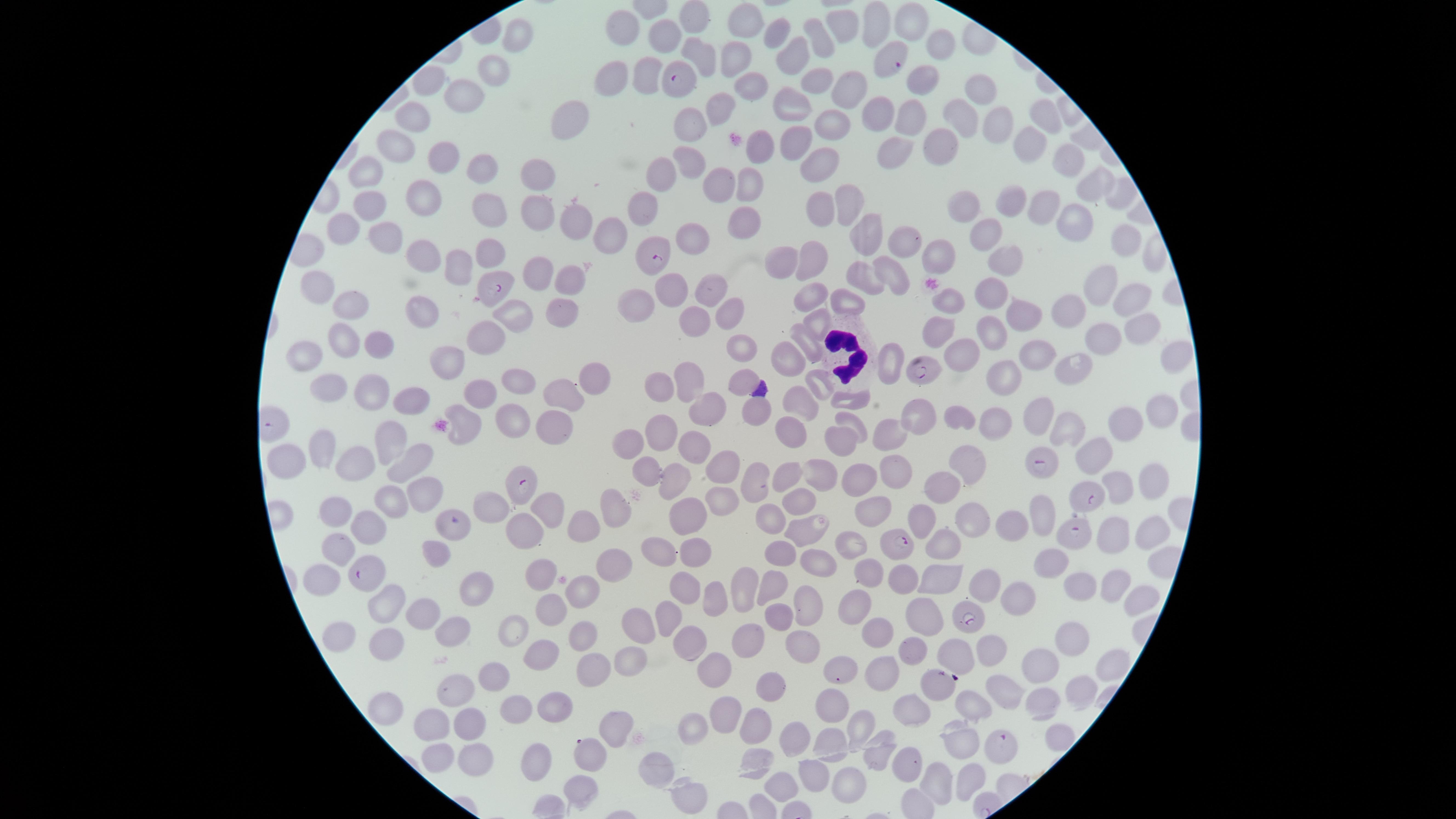
Approximate marker points as {x, y} in pixels.
Summary:
  - Uninfected red blood cells: {690, 19}, {870, 21}, {746, 22}, {906, 22}, {841, 23}, {622, 30}, {517, 33}, {667, 35}, {770, 37}, {820, 39}, {938, 46}, {698, 50}, {792, 57}, {738, 62}, {492, 71}, {654, 72}, {920, 73}, {614, 79}, {813, 81}, {750, 82}, {424, 85}, {841, 87}, {979, 88}, {462, 95}, {721, 108}, {790, 108}, {966, 110}, {1040, 116}, {415, 118}, {912, 118}, {877, 120}, {995, 122}, {569, 123}, {687, 125}, {831, 126}, {797, 140}, {1024, 141}, {935, 145}, {763, 146}, {396, 147}, {891, 147}, {687, 156}, {443, 157}, {1065, 158}, {820, 161}, {481, 168}, {661, 172}, {365, 179}, {537, 180}, {751, 181}, {1092, 185}, {721, 187}, {1118, 195}, {424, 198}, {493, 202}, {847, 202}, {1012, 202}, {365, 206}, {646, 206}, {1041, 208}, {968, 210}, {818, 211}, {535, 217}, {573, 222}, {741, 224}, {1071, 225}, {346, 228}, {867, 230}, {608, 233}, {983, 233}, {691, 240}, {381, 241}, {907, 242}, {1125, 246}, {492, 252}, {414, 255}, {934, 256}, {1009, 256}, {780, 257}, {809, 262}, {450, 264}, {545, 271}, {864, 276}, {569, 277}, {895, 279}, {1095, 286}, {714, 288}, {316, 291}, {667, 294}, {810, 294}, {994, 296}, {847, 300}, {956, 301}, {1122, 301}, {631, 304}, {358, 307}, {424, 309}, {1070, 309}, {563, 313}, {522, 314}, {729, 315}, {1030, 315}, {814, 318}, {693, 319}, {992, 325}, {1141, 330}, {496, 331}, {936, 332}, {1108, 339}, {375, 341}, {808, 341}, {347, 345}, {738, 350}, {1034, 351}, {792, 354}, {1171, 355}, {964, 356}, {1074, 362}, {888, 363}, {304, 365}, {454, 369}, {684, 375}, {1000, 377}, {515, 381}, {587, 381}, {739, 382}, {657, 384}, {327, 385}, {366, 386}, {817, 386}, {485, 391}, {422, 394}, {555, 401}, {848, 401}, {797, 402}, {706, 408}, {752, 412}, {919, 414}, {957, 414}, {1036, 415}, {506, 416}, {1163, 418}, {996, 421}, {851, 422}, {546, 424}, {1124, 424}, {469, 426}, {1066, 428}, {791, 431}, {668, 432}, {889, 433}, {843, 439}, {324, 447}, {628, 447}, {392, 449}, {687, 451}, {1093, 452}, {969, 461}, {292, 462}, {416, 464}, {890, 464}, {363, 466}, {647, 469}, {726, 469}, {1152, 474}, {787, 477}, {815, 477}, {756, 480}, {859, 482}, {1122, 482}, {674, 484}, {943, 486}, {425, 499}, {387, 500}, {722, 500}, {793, 500}, {872, 508}, {548, 511}, {617, 511}, {335, 512}, {1042, 512}, {485, 514}, {769, 516}, {924, 516}, {978, 519}, {689, 521}, {363, 522}, {1008, 523}, {1153, 526}, {584, 529}, {529, 530}, {1117, 530}, {805, 531}, {854, 543}, {335, 546}, {939, 546}, {695, 551}, {439, 553}, {656, 553}, {782, 553}, {615, 561}, {821, 566}, {866, 572}, {543, 574}, {325, 576}, {937, 578}, {899, 579}, {1081, 579}, {1113, 579}, {773, 582}, {685, 584}, {981, 585}, {751, 587}, {473, 589}, {579, 591}, {714, 594}, {1005, 597}, {1135, 598}, {388, 600}, {809, 601}, {551, 609}, {859, 613}, {425, 614}, {926, 614}, {665, 619}, {781, 619}, {646, 624}, {874, 629}, {456, 632}, {1069, 632}, {339, 634}, {580, 634}, {751, 634}, {516, 635}, {384, 637}, {691, 638}, {805, 646}, {987, 646}, {912, 651}, {548, 653}, {956, 656}, {1041, 659}, {632, 660}, {1108, 665}, {714, 670}, {600, 671}, {884, 671}, {845, 673}, {497, 677}, {1080, 686}, {774, 687}, {1010, 690}, {460, 698}, {1042, 701}, {829, 703}, {516, 706}, {979, 708}, {386, 709}, {914, 709}, {555, 710}, {722, 714}, {753, 723}, {467, 725}, {697, 726}, {859, 726}, {436, 727}, {615, 729}, {792, 737}, {962, 738}, {1056, 742}, {831, 749}, {873, 752}, {481, 757}, {909, 760}, {436, 761}, {753, 763}, {538, 764}, {667, 769}, {816, 771}, {582, 778}, {936, 778}, {970, 781}, {842, 783}, {787, 785}, {683, 792}
  - Parasitized red blood cells: {885, 63}, {683, 79}, {657, 255}, {495, 288}, {924, 368}, {1046, 465}, {522, 480}, {1091, 502}, {1075, 538}, {903, 544}, {365, 573}, {971, 618}, {935, 683}, {999, 748}, {588, 751}
  - White blood cells: {844, 353}
  - Species: Plasmodium falciparum
  - Visible region: circular
  - Presence: malaria parasites seen
  - Image size: 1456×819 pixels
  - Preparation: thin blood film
  - Field of view: single
  - Stain: Giemsa
  - Capture: smartphone photograph through the microscope eyepiece